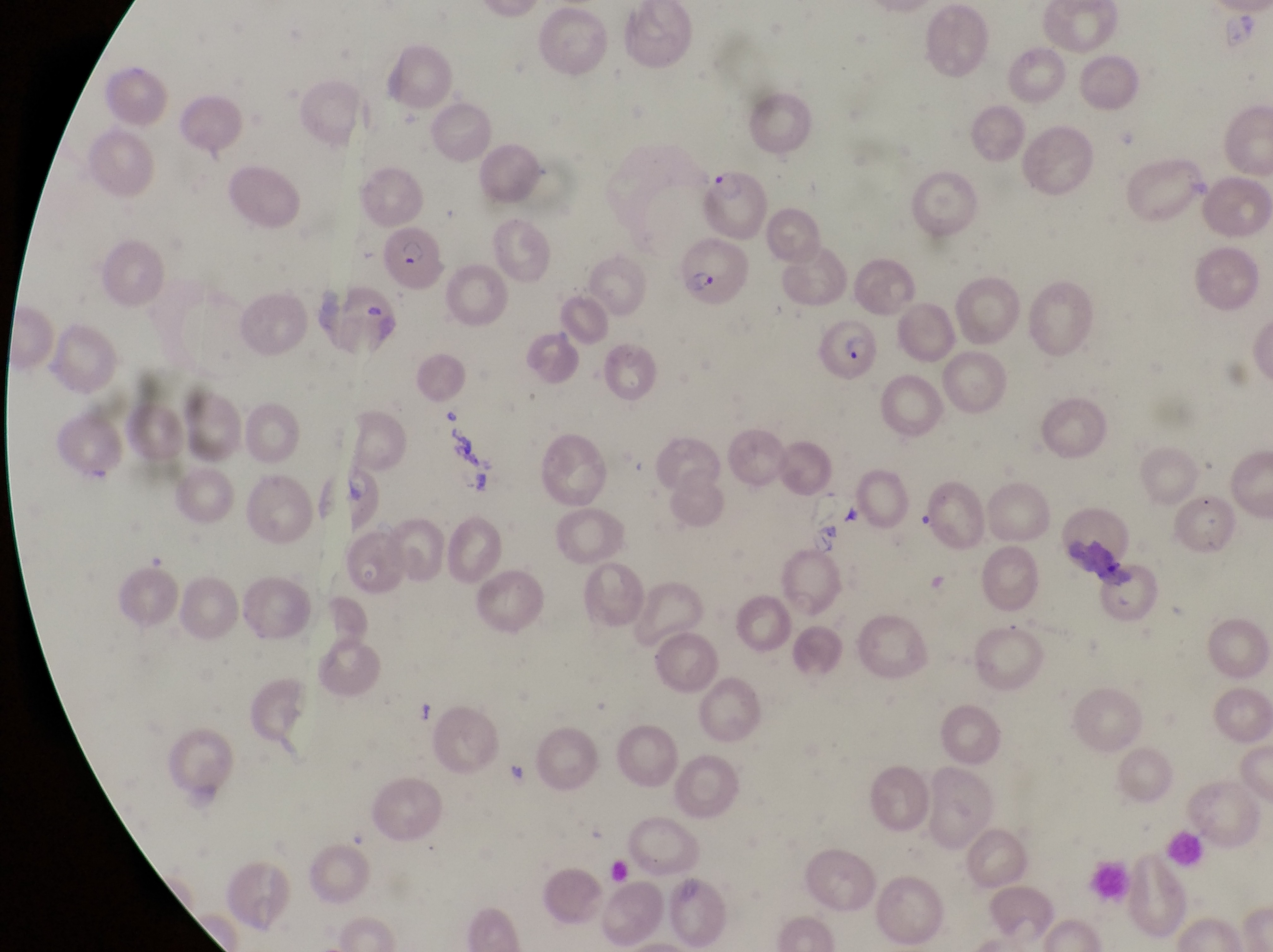

Approximate bounding boxes as (left, top, right, bottom) in pixels. Parasitised red blood cell locations: (701, 164, 764, 244), (382, 223, 447, 293), (681, 240, 751, 310), (817, 315, 882, 389). Single field of view. Image is 1273×952 pixels. Magnification of 1000x. Captured by a smartphone held over the eyepiece of an Olympus CX-23 microscope. Thin blood film. Collected in Uganda.